Locate every leukocyte (white blood cell).
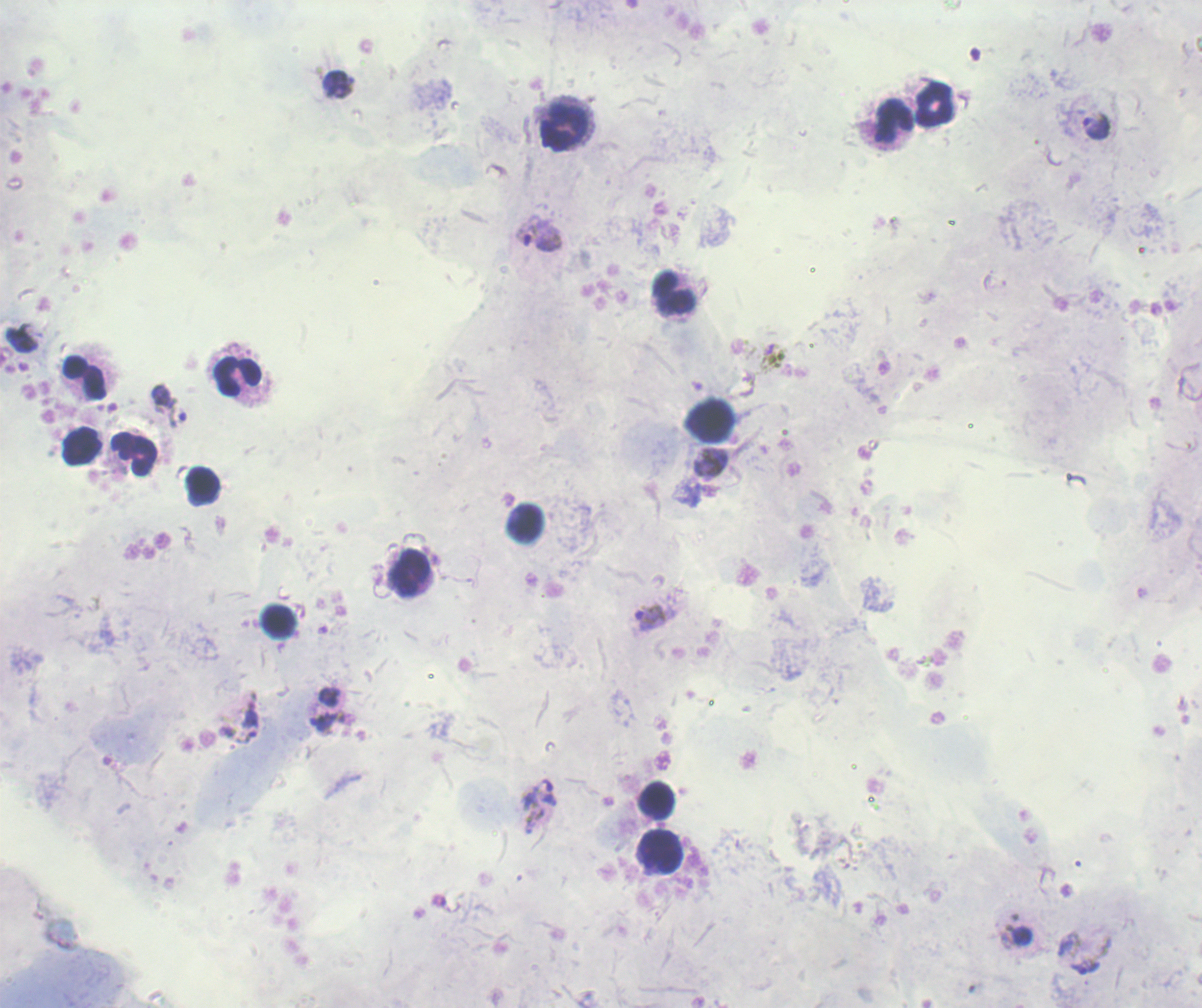

Approximate centers as {x, y} in pixels.
Leukocytes: {933, 104}, {893, 121}, {565, 126}, {673, 296}, {237, 376}, {87, 379}, {709, 420}, {81, 446}, {135, 454}, {203, 486}, {524, 523}, {409, 575}, {278, 623}, {656, 800}, {659, 853}.

Approximate centers as {x, y} in pixels. Trophozoite locations: {338, 84}, {1095, 127}, {539, 234}, {22, 339}, {162, 396}, {178, 413}, {710, 462}, {650, 616}, {329, 697}, {323, 720}, {249, 723}, {540, 805}, {1086, 967}. Image is 1202×1008 pixels. Thick smear of blood. Background quality: poor. Romanowsky stain. Result: malaria parasites identified. Previously used in a real diagnosis. One field from this slide. 100x magnification.